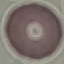

Result: negative for malaria parasites. Giemsa-stained preparation. Thin smear of blood. Cell patch, automatically extracted from a larger field of view and resized to 64 × 64 pixels. Photographed with a smartphone camera at the microscope eyepiece.